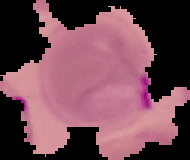

From a thin blood film. Image is 190×160 pixels. Segmented cell region on a black background. Result: malaria parasites identified.